Assess this cell for malaria.
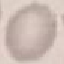
It is uninfected.

Summary:
  - Stain: Giemsa
  - Image type: cell patch, automatically extracted from a larger field of view and resized to 64 × 64 pixels
  - Preparation: thin blood film
  - Capture: smartphone through the microscope eyepiece